Report the malaria status of this cell.
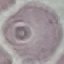

It is uninfected.

Photographed with a smartphone camera at the microscope eyepiece. Thin blood smear. Cell patch, automatically extracted from a larger field of view and resized to 64 × 64 pixels. Giemsa stain.